Classify this cell by malaria status.
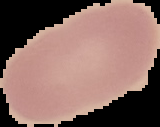

It is uninfected.

{
  "image_size": "160×127 pixels",
  "image_type": "segmented cell region with the area outside set to black",
  "preparation": "thin blood film"
}